Name the cell type shown.
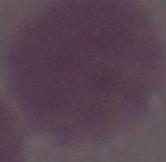

An erythrocyte.

Summary:
  - Magnification: 1000x
  - Modality: micrograph